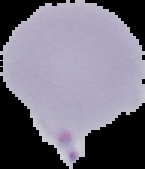 Malaria status: parasitized. The area outside the segmented cell region is set to black. From a thin blood film. Image is 145×169 pixels.